Give the preparation type.
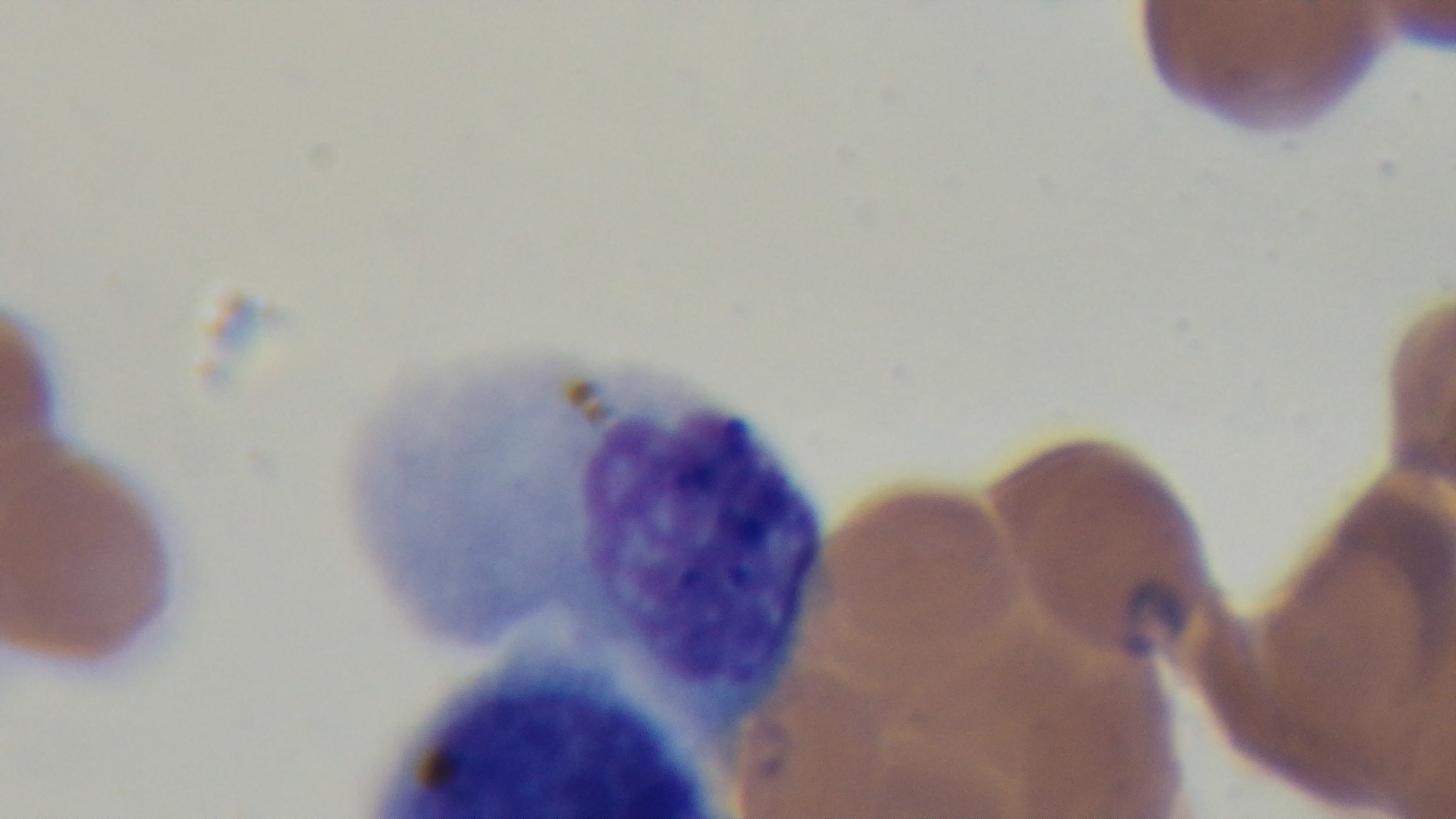
It is a thin blood film.

Giemsa-stained. Single field of view. Malaria status: infected. Light microscopy. Captured with a mounted 4K digital camera. Oil-immersion objective, 100x.